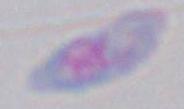
magnification = 1000x
identification = Toxoplasma gondii
modality = photomicrograph